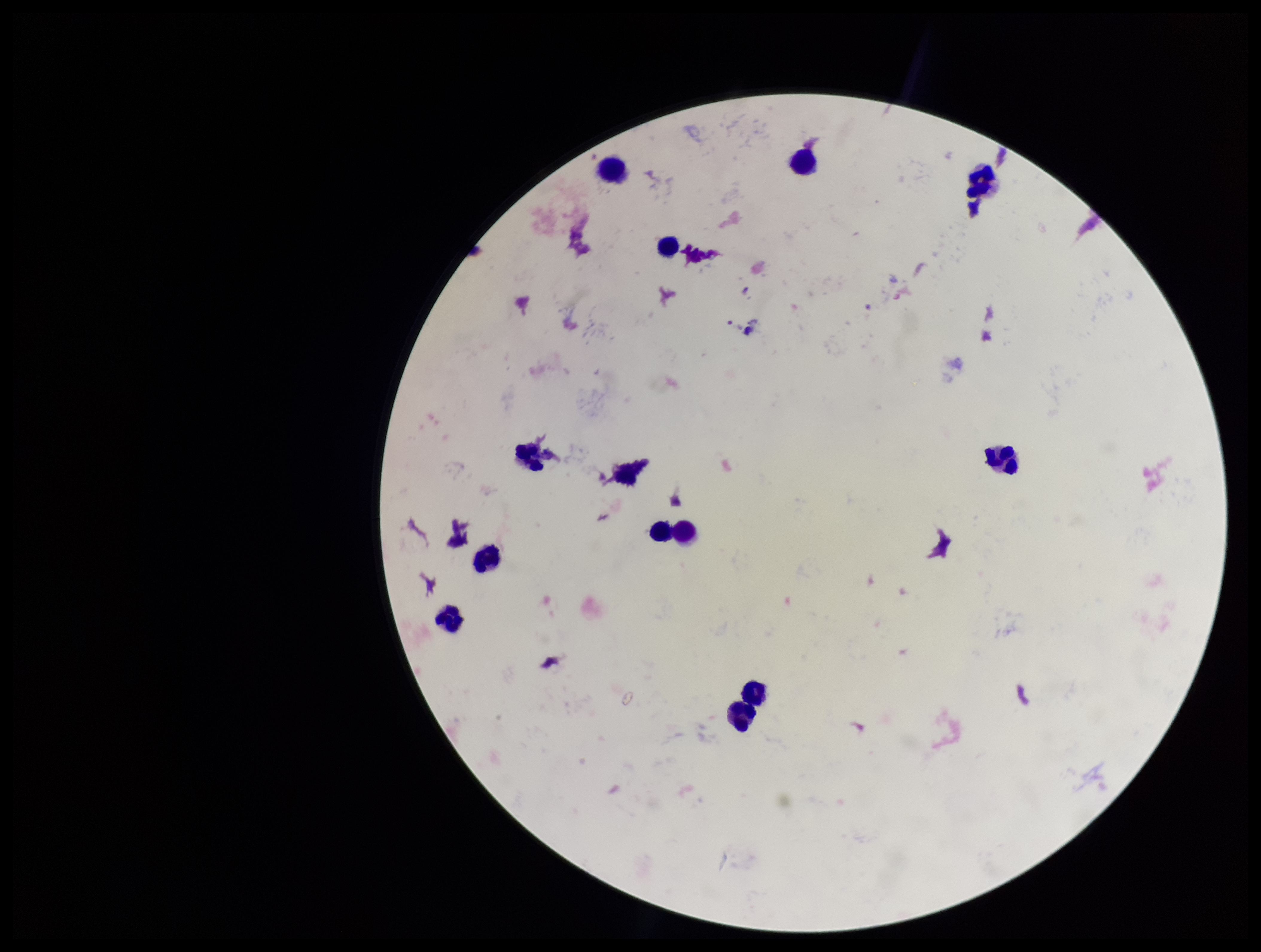
Summary:
  - Leukocyte count: 13
  - Image size: 1261×952 pixels
  - Plasmodium parasites: none detected
  - Parasite count: 0
  - Field of view: one from this slide
  - Capture: smartphone photograph through the microscope eyepiece
  - Patient malaria status: negative
  - Preparation: thick smear
  - Stain: Giemsa